Report the malaria status of this cell.
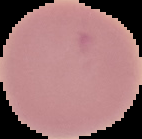

Uninfected.

Summary:
  - Image size: 142×139 pixels
  - Preparation: thin blood film
  - Image type: segmented cell region on a black background